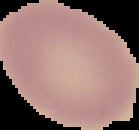
image type = segmented cell region with the area outside set to black
image size = 139×130 pixels
result = negative for Plasmodium parasites
preparation = thin blood smear